State the blood parasite species.
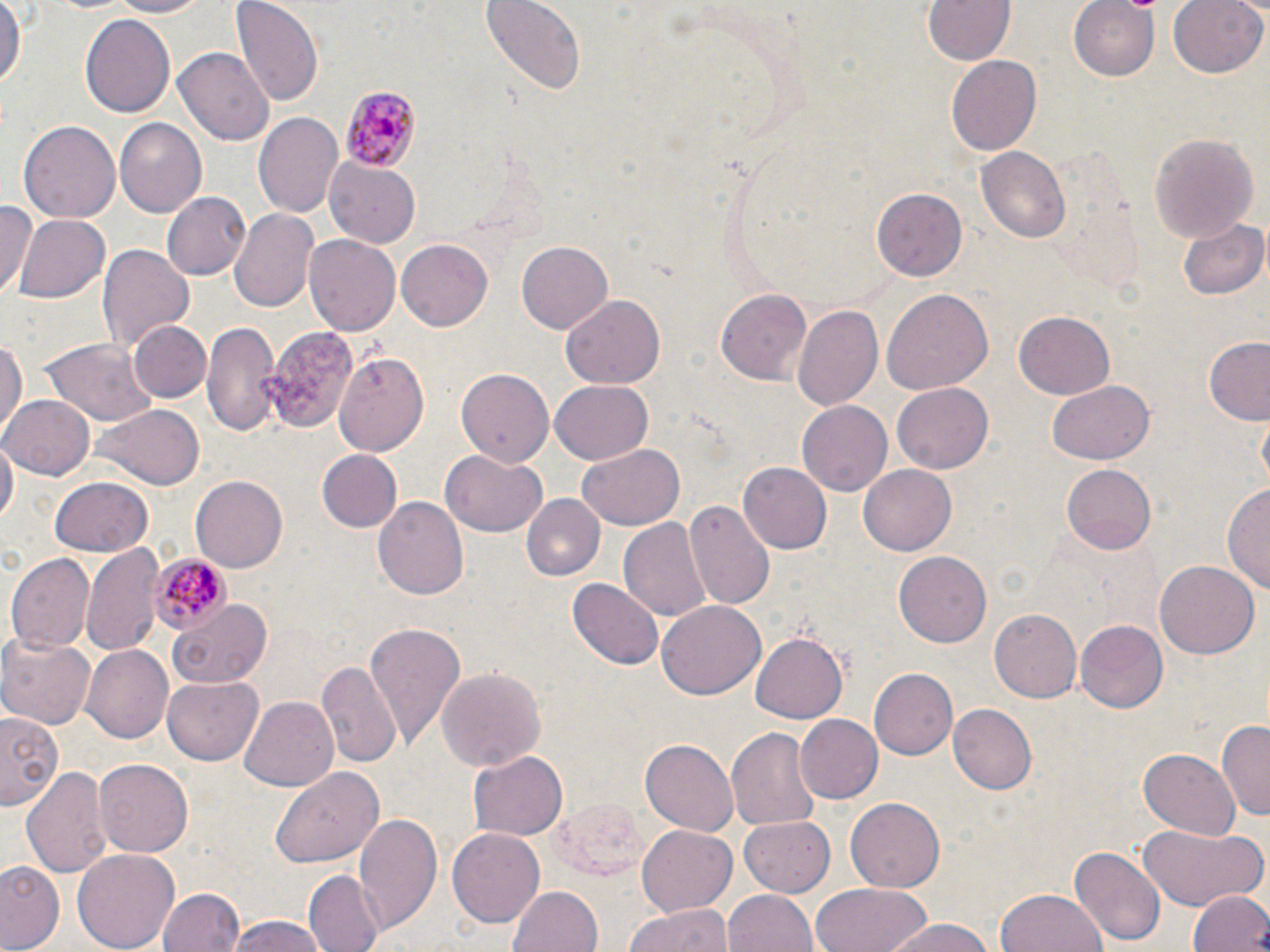

Plasmodium malariae.

field_of_view: single
plasmodium_malariae_infected_red_blood_cell_locations: 'approximate bounding boxes as (x1, y1, x2, y2) in pixels: (339, 88, 419, 170), (149, 553, 231, 636)'
stain: May-Grünwald-Giemsa
magnification: 1000x
image_size: 1270×952 pixels
modality: optical microscopy
uninfected_red_blood_cell_locations: 'approximate bounding boxes as (x1, y1, x2, y2) in pixels: (0, 0, 23, 94), (104, 0, 210, 19), (478, 0, 588, 94), (919, 0, 1018, 65), (1070, 0, 1161, 81), (1167, 0, 1268, 78), (233, 1, 322, 106), (80, 11, 178, 117), (175, 48, 274, 147), (944, 54, 1043, 158), (254, 111, 344, 221), (115, 118, 207, 218), (19, 120, 120, 225), (1146, 129, 1260, 243), (975, 147, 1071, 244), (325, 159, 421, 249), (871, 188, 967, 281), (162, 192, 252, 280), (2, 201, 37, 299), (230, 208, 319, 313), (12, 212, 112, 305), (1179, 219, 1268, 301), (306, 234, 399, 336), (394, 236, 494, 330), (516, 239, 613, 333), (99, 244, 194, 352), (714, 287, 812, 386), (883, 289, 995, 393), (560, 296, 662, 389), (791, 304, 884, 414), (1014, 312, 1115, 399), (202, 319, 283, 435), (127, 321, 211, 405), (265, 325, 356, 431), (1201, 334, 1270, 423), (0, 336, 27, 439), (43, 338, 157, 428), (334, 351, 429, 453), (456, 368, 553, 467), (893, 380, 993, 471), (548, 381, 654, 466), (1046, 381, 1153, 466), (0, 392, 95, 480), (798, 401, 892, 494), (93, 404, 204, 488), (1, 437, 16, 533), (576, 445, 684, 530), (315, 450, 402, 533), (442, 452, 547, 536), (739, 460, 832, 552), (1058, 463, 1160, 555), (861, 464, 956, 554), (49, 477, 152, 556), (191, 477, 288, 571), (1223, 482, 1270, 594), (520, 493, 605, 581), (372, 496, 469, 602), (686, 499, 775, 608), (619, 518, 711, 624), (80, 544, 164, 659), (7, 551, 95, 652), (895, 551, 992, 646), (1154, 560, 1258, 658), (569, 577, 663, 670), (165, 596, 275, 688), (658, 602, 764, 699), (988, 609, 1081, 703), (1073, 620, 1166, 713), (363, 621, 467, 747), (750, 632, 848, 724), (0, 633, 95, 729), (80, 644, 176, 743), (316, 660, 400, 768), (437, 667, 546, 773), (867, 668, 958, 760), (162, 678, 265, 765), (240, 696, 339, 792), (947, 703, 1035, 792), (0, 714, 63, 807), (793, 714, 882, 804), (1219, 721, 1270, 822), (725, 725, 821, 830), (642, 740, 737, 836), (1137, 748, 1241, 839), (469, 750, 567, 840), (94, 760, 193, 855), (21, 765, 113, 880), (270, 765, 384, 868), (543, 795, 652, 880), (846, 797, 945, 890), (355, 813, 441, 932), (740, 815, 835, 898), (1138, 822, 1267, 912), (636, 825, 737, 917), (448, 827, 545, 928), (1070, 843, 1165, 949), (69, 848, 180, 952), (0, 860, 64, 950), (304, 869, 381, 952), (817, 883, 934, 952), (508, 884, 604, 952), (158, 888, 244, 952), (723, 889, 818, 952), (1188, 889, 1270, 952), (998, 891, 1107, 952), (626, 901, 732, 952), (223, 916, 333, 952), (881, 917, 993, 952)'
preparation: thin blood smear